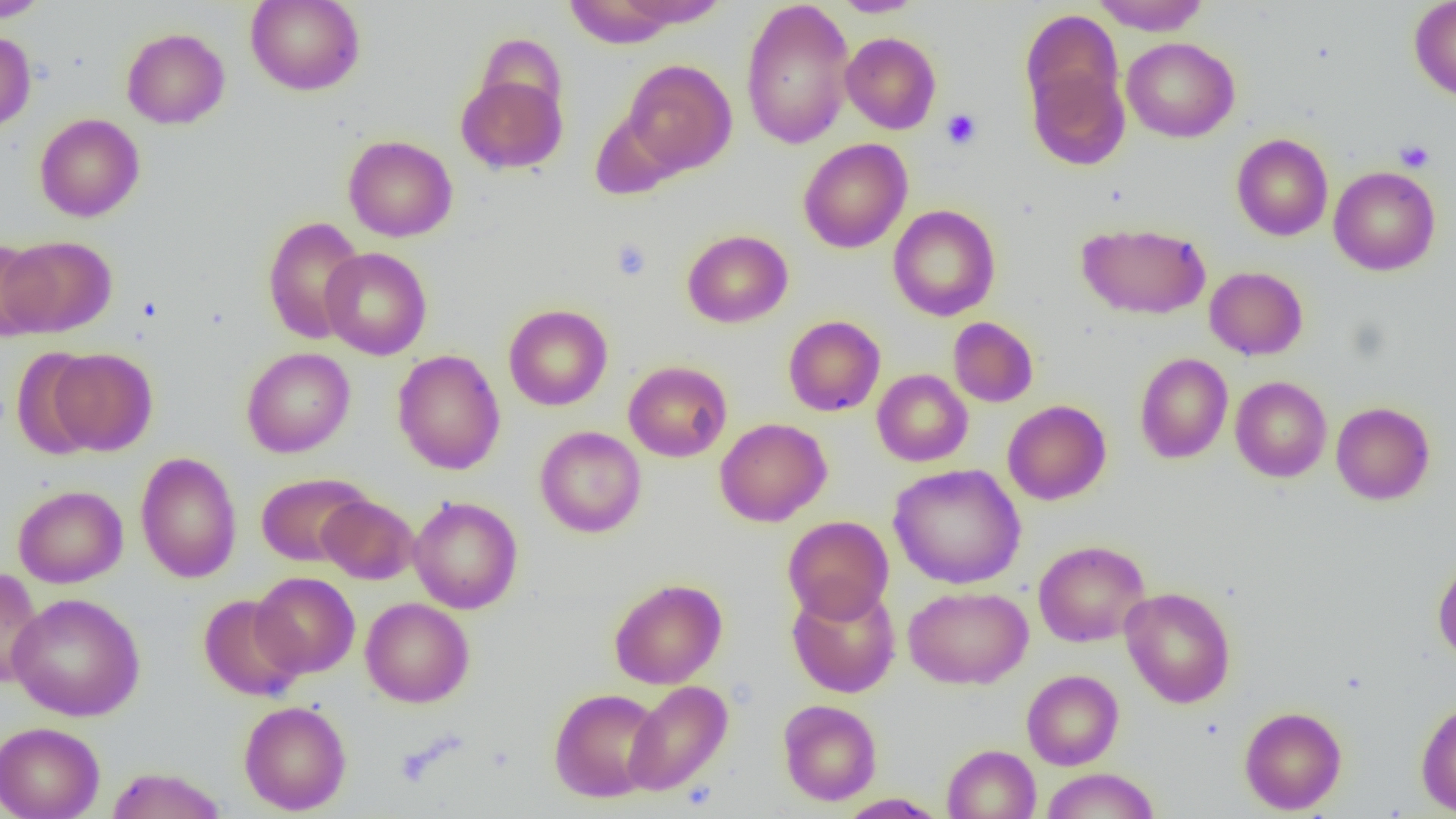 Approximate bounding boxes as named x1/y1/x2/y2 corners in pixels. Uninfected red blood cell locations: (x1=0, y1=0, x2=51, y2=22), (x1=246, y1=0, x2=365, y2=96), (x1=618, y1=0, x2=730, y2=28), (x1=740, y1=0, x2=855, y2=150), (x1=1091, y1=0, x2=1210, y2=35), (x1=1409, y1=0, x2=1456, y2=102), (x1=564, y1=1, x2=681, y2=49), (x1=831, y1=1, x2=926, y2=17), (x1=1021, y1=10, x2=1124, y2=122), (x1=121, y1=27, x2=230, y2=129), (x1=0, y1=30, x2=36, y2=133), (x1=840, y1=32, x2=941, y2=134), (x1=1122, y1=37, x2=1239, y2=142), (x1=623, y1=59, x2=736, y2=175), (x1=1026, y1=60, x2=1130, y2=171), (x1=455, y1=72, x2=567, y2=175), (x1=589, y1=109, x2=684, y2=200), (x1=34, y1=113, x2=145, y2=222), (x1=1231, y1=133, x2=1333, y2=241), (x1=343, y1=135, x2=457, y2=242), (x1=797, y1=138, x2=913, y2=254), (x1=1329, y1=166, x2=1440, y2=276), (x1=888, y1=205, x2=1000, y2=321), (x1=262, y1=215, x2=367, y2=344), (x1=1077, y1=222, x2=1211, y2=319), (x1=682, y1=229, x2=793, y2=328), (x1=3, y1=235, x2=117, y2=337), (x1=0, y1=239, x2=51, y2=340), (x1=320, y1=247, x2=432, y2=360), (x1=1204, y1=266, x2=1308, y2=360), (x1=503, y1=304, x2=613, y2=411), (x1=783, y1=315, x2=885, y2=416), (x1=948, y1=317, x2=1038, y2=407), (x1=11, y1=347, x2=102, y2=460), (x1=242, y1=347, x2=356, y2=458), (x1=48, y1=348, x2=157, y2=456), (x1=392, y1=349, x2=506, y2=475), (x1=1134, y1=353, x2=1233, y2=464), (x1=623, y1=360, x2=732, y2=462), (x1=872, y1=369, x2=973, y2=466), (x1=1231, y1=376, x2=1331, y2=482), (x1=1002, y1=400, x2=1111, y2=505), (x1=1331, y1=401, x2=1435, y2=505), (x1=715, y1=418, x2=831, y2=526), (x1=535, y1=426, x2=646, y2=538), (x1=135, y1=452, x2=242, y2=583), (x1=888, y1=464, x2=1026, y2=589), (x1=255, y1=472, x2=374, y2=567), (x1=13, y1=484, x2=128, y2=588), (x1=317, y1=494, x2=419, y2=584), (x1=408, y1=496, x2=523, y2=614), (x1=782, y1=515, x2=894, y2=623), (x1=1033, y1=540, x2=1150, y2=647), (x1=1432, y1=555, x2=1456, y2=663), (x1=0, y1=567, x2=44, y2=689), (x1=251, y1=572, x2=360, y2=678), (x1=609, y1=578, x2=727, y2=689), (x1=787, y1=582, x2=900, y2=698), (x1=903, y1=585, x2=1033, y2=689), (x1=1120, y1=586, x2=1236, y2=708), (x1=8, y1=593, x2=146, y2=721), (x1=198, y1=594, x2=305, y2=702), (x1=360, y1=597, x2=474, y2=707), (x1=1022, y1=669, x2=1124, y2=770), (x1=623, y1=680, x2=733, y2=796), (x1=549, y1=688, x2=664, y2=802), (x1=778, y1=699, x2=882, y2=805), (x1=1415, y1=699, x2=1456, y2=816), (x1=239, y1=700, x2=352, y2=815), (x1=1239, y1=706, x2=1347, y2=814), (x1=0, y1=722, x2=105, y2=819), (x1=942, y1=744, x2=1041, y2=819), (x1=105, y1=766, x2=227, y2=819), (x1=1040, y1=768, x2=1160, y2=819), (x1=836, y1=793, x2=948, y2=818). Platelet locations: (x1=941, y1=108, x2=982, y2=150), (x1=1395, y1=139, x2=1435, y2=172), (x1=611, y1=239, x2=652, y2=281). Slide-level diagnosis: negative for blood parasites. Light microscopy. 1000x magnification. Thin blood film. Single field of view. Image is 1456×819 pixels.